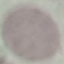
Summary:
  - Malaria status: uninfected
  - Capture: smartphone camera at the microscope eyepiece
  - Preparation: thin blood smear
  - Image type: automatically extracted cell patch, resized to 64 × 64 pixels
  - Stain: Giemsa